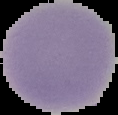
preparation = thin blood smear
result = Plasmodium parasites identified
image type = segmented cell region with the area outside set to black
image size = 118×115 pixels